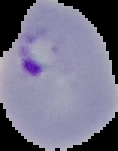
The area outside the segmented cell region is set to black. From a thin blood film. Image is 118×151 pixels. Result: Plasmodium parasites detected.